Report the malaria status of this cell.
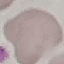

It is uninfected.

image_type: automatically extracted cell patch, resized to 64 × 64 pixels
preparation: thin smear
stain: Giemsa
capture: smartphone through the microscope eyepiece